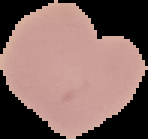

From a thin blood film. Image is 148×139 pixels. Malaria status: uninfected. Cell region segmented out of the field of view; the surrounding area is masked to black.